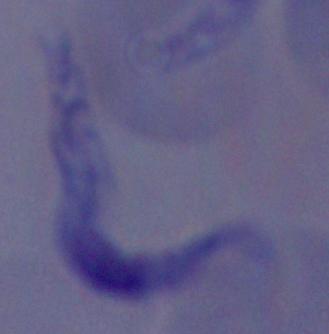
{
  "magnification": "1000x",
  "modality": "micrograph",
  "identification": "trypanosome"
}